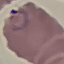
result = malaria parasites identified
stain = Giemsa
image type = automatically extracted cell patch, resized to 64 × 64 pixels
preparation = thin blood film
capture = smartphone camera at the microscope eyepiece